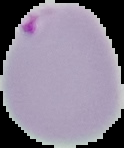

The area outside the segmented cell region is set to black. Image is 124×148 pixels. Result: malaria parasites identified. From a thin blood smear.